State which parasite is depicted.
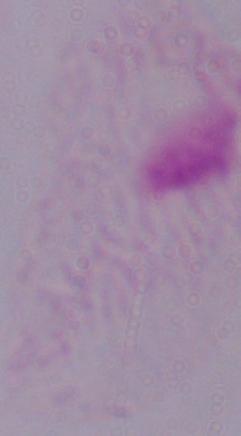
This is a trichomonad.

Summary:
  - Modality: micrograph
  - Magnification: 1000x